Locate every Plasmodium vivax-infected red blood cell.
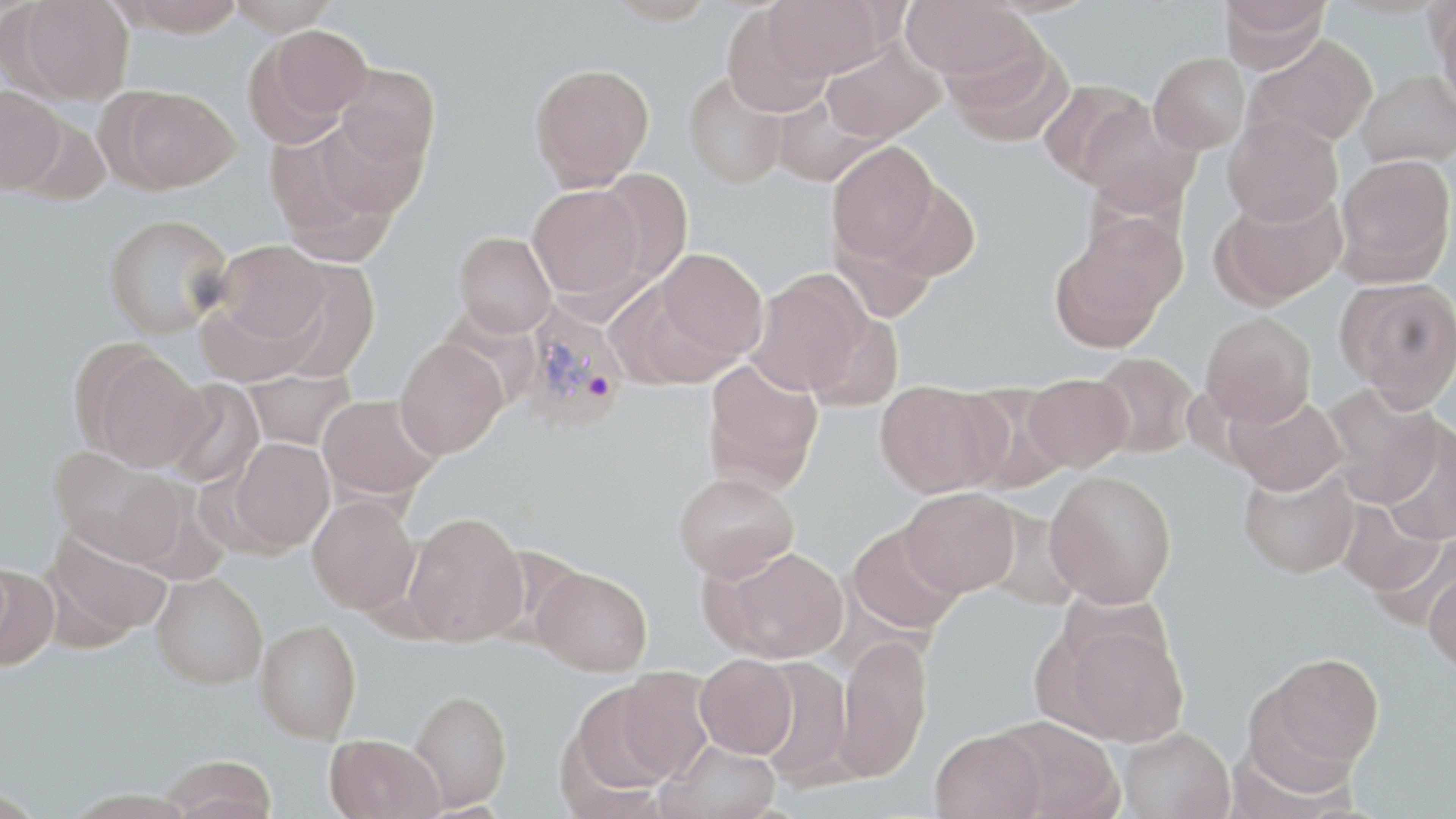

Approximate bounding boxes as (x1,y1)-(x2,y2) corner pairs in pixels.
Plasmodium vivax-infected red blood cells: (517,300)-(630,435).

Uninfected red blood cell locations: (14,0)-(134,104), (115,0)-(246,36), (224,0)-(340,36), (603,0)-(717,25), (765,0)-(889,80), (901,0)-(1036,82), (1219,0)-(1331,68), (1431,2)-(1456,109), (722,6)-(833,118), (248,24)-(372,144), (1246,35)-(1378,148), (942,37)-(1073,145), (822,39)-(945,143), (1149,52)-(1250,154), (530,62)-(654,190), (334,64)-(440,169), (1356,70)-(1456,168), (683,71)-(788,189), (1038,81)-(1150,186), (0,85)-(67,193), (111,86)-(242,192), (771,93)-(884,186), (1075,99)-(1201,216), (12,113)-(113,206), (1223,114)-(1343,227), (266,124)-(407,262), (826,141)-(940,266), (1334,153)-(1455,283), (593,168)-(693,284), (876,179)-(981,282), (527,184)-(645,301), (1211,189)-(1347,308), (102,213)-(233,339), (1053,215)-(1183,346), (454,231)-(557,336), (210,239)-(331,355), (651,248)-(767,366), (262,259)-(380,381), (746,270)-(871,397), (1336,277)-(1456,408), (1200,312)-(1316,427), (394,339)-(507,458), (81,345)-(208,471), (1090,351)-(1200,458), (701,358)-(824,495), (242,368)-(357,450), (1023,373)-(1132,471), (163,381)-(265,489), (875,381)-(1002,497), (1322,383)-(1444,508), (957,385)-(1070,493), (1224,391)-(1346,495), (317,394)-(440,500), (1380,423)-(1456,545), (228,437)-(334,553), (48,446)-(190,566), (1238,463)-(1360,578), (1045,469)-(1177,608), (673,472)-(799,581), (900,488)-(1020,597), (308,494)-(421,614), (1337,498)-(1447,600), (403,511)-(529,645), (847,523)-(964,635), (42,525)-(171,648), (713,546)-(849,662), (0,560)-(58,670), (1425,560)-(1456,677), (532,567)-(652,676), (151,572)-(268,689), (1047,615)-(1189,745), (255,619)-(362,743), (833,635)-(932,781), (1251,652)-(1384,783), (695,654)-(798,758), (755,656)-(855,786), (611,668)-(715,782), (565,681)-(682,797), (409,689)-(511,810), (991,716)-(1123,819), (1117,727)-(1235,819), (930,728)-(1047,819), (325,734)-(444,819), (658,739)-(784,818), (162,754)-(279,819). Slide-level diagnosis: Plasmodium vivax. May-Grünwald-Giemsa-stained preparation. Optical microscopy. Single field of view. Image is 1456×819 pixels. Thin blood film. 1000x magnification.